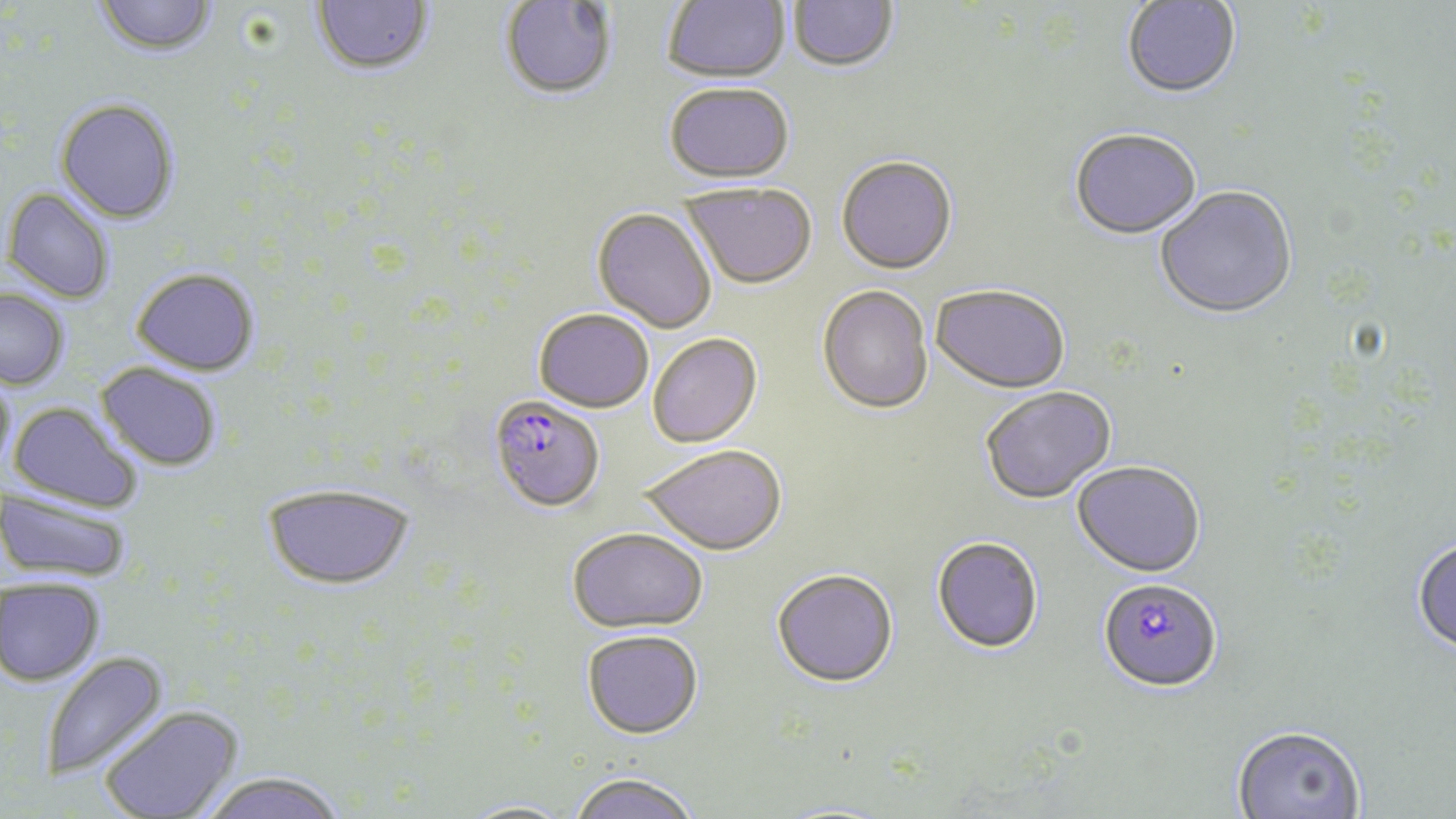 Approximate bounding boxes as (x1, y1, x2, y2) in pixels. Plasmodium falciparum-infected red blood cell locations: (488, 394, 605, 513), (1098, 577, 1222, 692). Uninfected red blood cell locations: (93, 0, 218, 56), (310, 0, 433, 75), (662, 0, 789, 82), (788, 0, 899, 72), (499, 1, 617, 100), (1121, 1, 1242, 98), (663, 82, 794, 182), (55, 97, 181, 223), (1069, 127, 1202, 240), (836, 155, 958, 275), (681, 183, 817, 290), (1155, 187, 1297, 320), (3, 188, 116, 304), (592, 207, 717, 334), (130, 268, 261, 375), (931, 285, 1070, 394), (817, 286, 933, 415), (0, 289, 69, 389), (534, 308, 654, 413), (647, 333, 762, 448), (95, 362, 223, 471), (0, 372, 16, 480), (980, 386, 1116, 505), (8, 401, 144, 514), (641, 445, 788, 556), (1072, 461, 1205, 578), (262, 482, 415, 589), (1, 485, 134, 585), (567, 527, 708, 633), (931, 536, 1044, 653), (1411, 537, 1456, 655), (772, 568, 899, 688), (1, 577, 104, 685), (582, 629, 704, 738), (40, 649, 169, 783), (98, 705, 244, 819), (1231, 724, 1367, 818), (196, 772, 350, 819), (568, 772, 700, 819), (457, 800, 577, 819). Slide-level diagnosis: Plasmodium falciparum. Optical microscopy. One field of a larger specimen. Thin blood smear. Image is 1456×819 pixels. May-Grünwald-Giemsa stain. 1000x magnification.